Name the parasite shown.
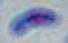

Toxoplasma gondii.

Micrograph. Captured at 1000x magnification.